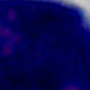
Micrograph. A white blood cell is shown. Captured at 1000x magnification.